Identify the parasite.
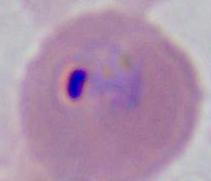
Plasmodium.

Photomicrograph. Captured at either 400x or 1000x magnification.